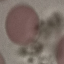

Summary:
  - Malaria status: uninfected
  - Capture: smartphone camera at the microscope eyepiece
  - Preparation: thin blood smear
  - Image type: cell patch, automatically extracted from a larger field of view and resized to 64 × 64 pixels
  - Stain: Giemsa